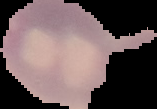

The area outside the segmented cell region is set to black. Result: malaria parasites detected. Image is 157×109 pixels. From a thin blood film.